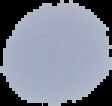
image size = 112×106 pixels
preparation = thin blood smear
malaria status = uninfected
image type = segmented cell region on a black background